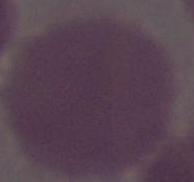

{
  "modality": "photomicrograph",
  "identification": "red blood cell",
  "magnification": "1000x"
}